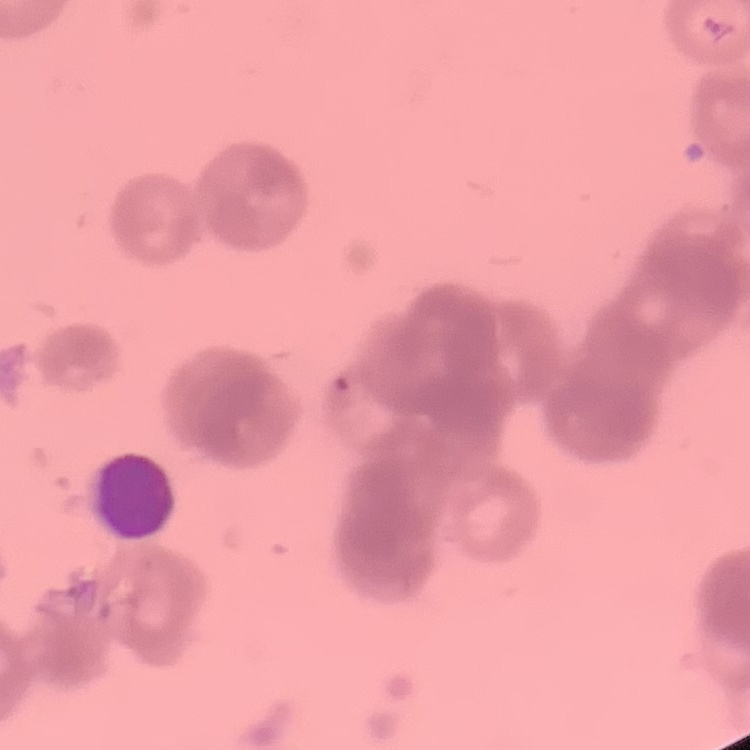

red_blood_cell_morphology: rouleaux formation
stain: Field's or Giemsa
preparation: thin peripheral smear
image_type: square crop of a larger photomicrograph